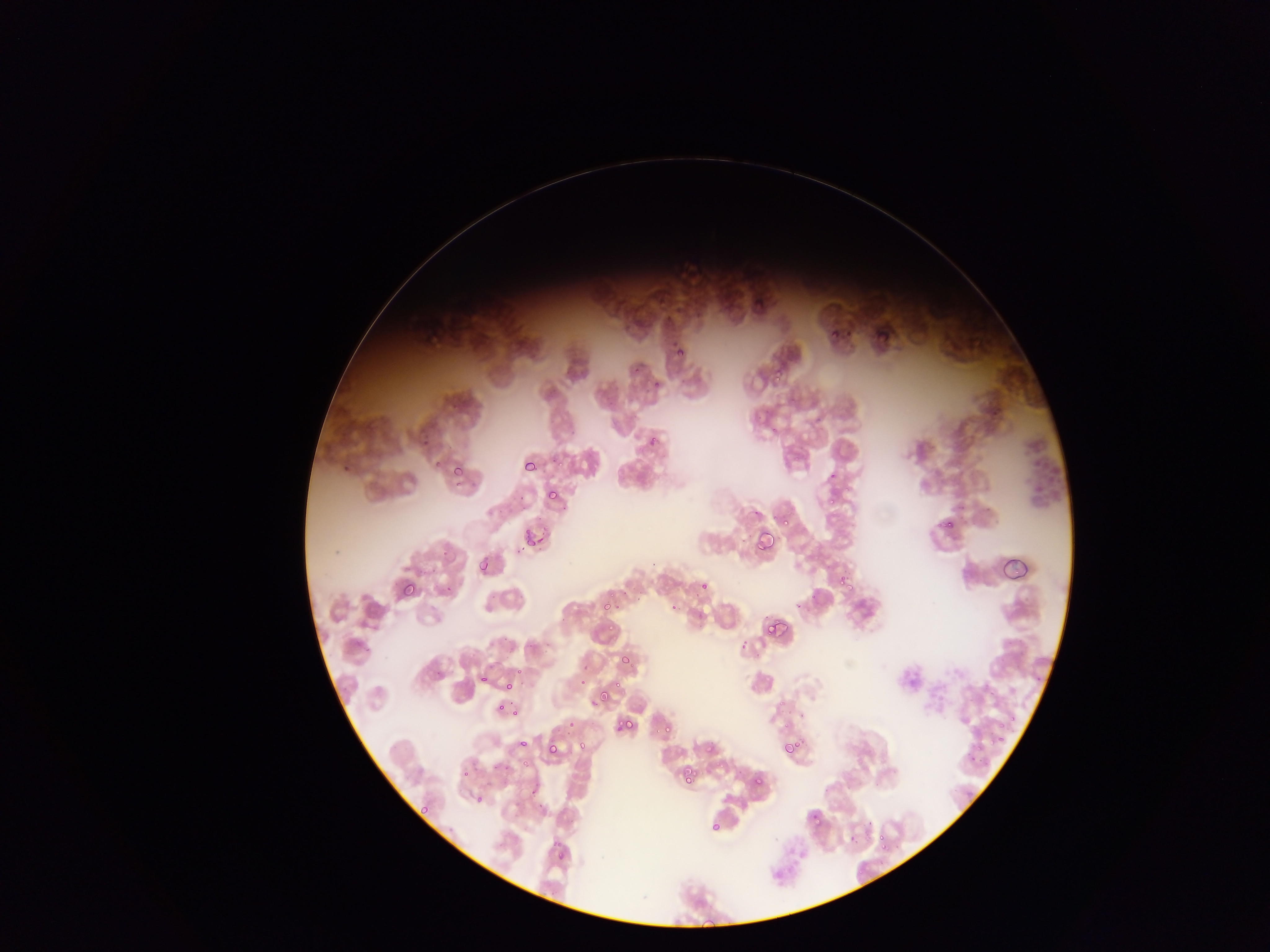
capture = mobile-phone photograph through a microscope
country = Ghana
image size = 1270×952 pixels
field of view = single
Plasmodium parasite locations = approximate bounding boxes as left top right bottom in pixels: 651 288 671 309; 426 320 447 342; 829 329 838 343; 773 367 781 383; 647 435 659 449; 423 437 433 452; 433 455 443 467; 523 458 539 474; 552 458 566 473; 452 466 462 476; 829 471 837 479; 451 482 462 491; 545 489 556 500; 825 497 835 504; 940 510 962 535; 778 514 791 527; 941 517 957 533; 754 530 777 555; 527 535 537 548; 480 560 492 572; 836 572 857 595; 701 577 710 592; 400 582 419 600; 443 583 456 597; 604 588 615 597; 603 606 611 612; 765 619 785 639; 605 622 616 631; 737 643 750 653; 619 651 634 668; 516 666 523 679; 477 675 486 685; 579 675 587 685; 594 681 617 707; 502 682 513 690; 591 689 611 709; 497 705 505 711; 996 709 1019 737; 512 711 520 720; 797 712 810 718; 565 713 573 730; 615 716 638 736; 781 721 790 728; 992 723 1011 748; 663 725 672 735; 518 730 532 748; 544 738 562 759; 780 739 798 758; 576 740 589 755; 704 742 718 757; 968 750 985 767; 520 758 530 765; 679 765 698 785; 461 769 472 780; 750 773 765 788; 475 795 486 806; 418 804 429 817; 809 810 826 828; 709 821 722 834; 846 832 859 845; 876 832 891 850; 553 843 568 864 | approximate x y pixel centers of objects too small to bound: 680 353; 673 607; 779 704
preparation = thin blood smear